Give the extent of all Plasmodium falciparum-infected red blood cells.
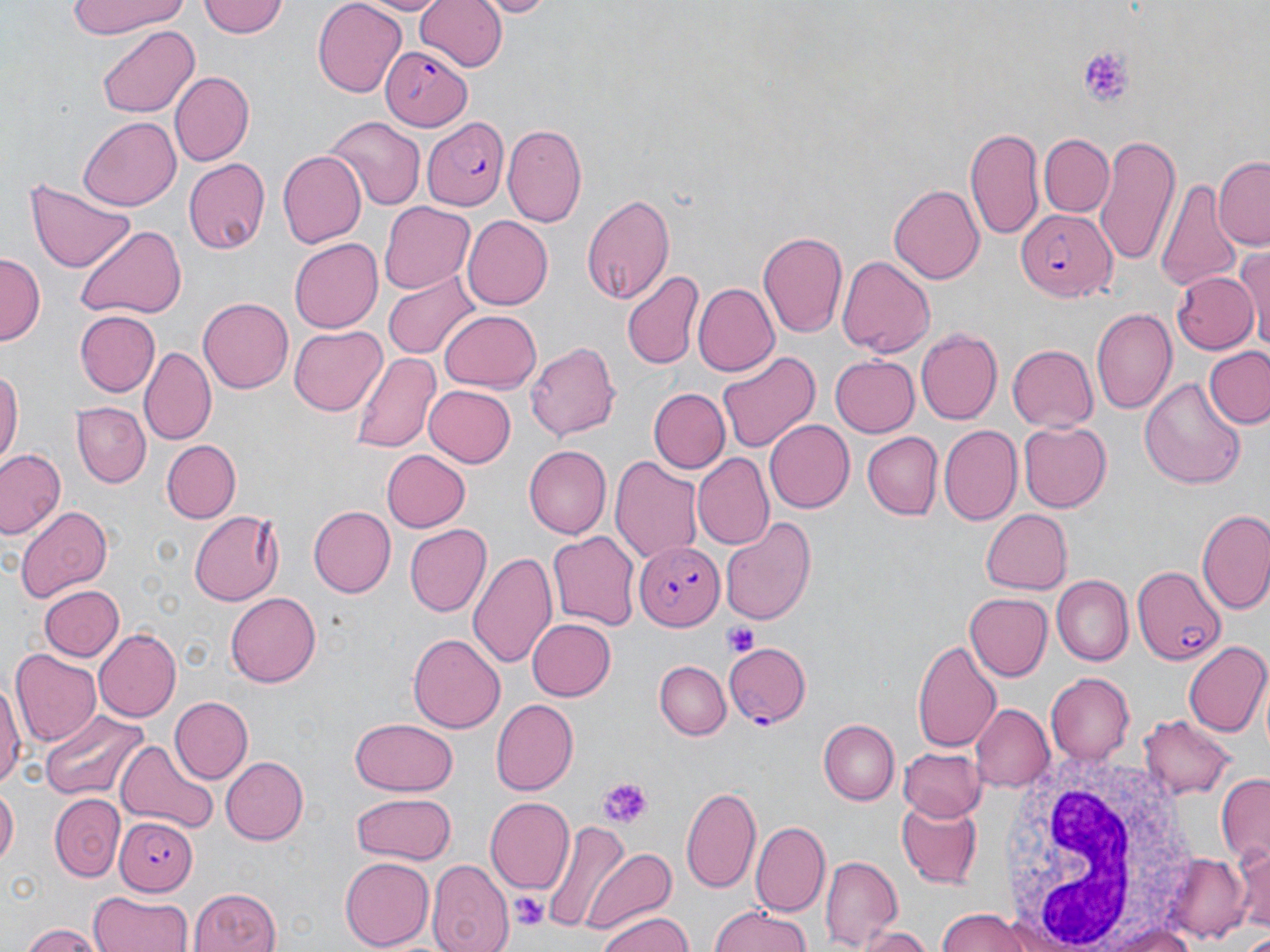

Approximate bounding boxes as (x1, y1, x2, y2) in pixels.
Plasmodium falciparum-infected red blood cells: (381, 47, 472, 131), (422, 118, 509, 211), (1018, 208, 1119, 299), (633, 542, 721, 630), (1132, 562, 1227, 667), (724, 640, 812, 728), (114, 814, 195, 894).

slide-level diagnosis = Plasmodium falciparum
modality = light microscopy
image size = 1270×952 pixels
preparation = thin blood film
stain = May-Grünwald-Giemsa
magnification = 1000x
platelet locations = approximate bounding boxes as (x1, y1, x2, y2) in pixels: (1077, 46, 1137, 107), (724, 622, 761, 658), (597, 779, 650, 824), (513, 893, 545, 930)
uninfected red blood cell locations = approximate bounding boxes as (x1, y1, x2, y2) in pixels: (67, 0, 194, 39), (199, 0, 289, 40), (312, 0, 406, 95), (355, 0, 452, 15), (414, 0, 508, 71), (475, 0, 555, 17), (97, 26, 199, 118), (170, 72, 254, 167), (81, 115, 180, 210), (325, 118, 422, 209), (502, 123, 588, 225), (964, 124, 1045, 239), (1040, 134, 1114, 217), (1093, 134, 1182, 270), (278, 149, 366, 250), (1215, 156, 1270, 248), (183, 158, 270, 255), (1157, 176, 1242, 295), (26, 180, 137, 273), (889, 182, 984, 285), (580, 191, 676, 304), (378, 201, 475, 295), (461, 215, 552, 310), (73, 225, 188, 322), (758, 231, 849, 341), (289, 238, 384, 333), (1234, 242, 1270, 348), (1, 253, 43, 346), (835, 254, 935, 359), (382, 267, 480, 360), (621, 269, 705, 370), (1170, 272, 1258, 354), (693, 282, 779, 377), (198, 296, 292, 391), (1092, 305, 1178, 417), (75, 311, 160, 395), (439, 311, 541, 394), (290, 326, 385, 414), (915, 329, 1003, 426), (525, 339, 622, 441), (1007, 344, 1098, 434), (140, 346, 215, 443), (1205, 347, 1270, 429), (715, 348, 822, 454), (350, 350, 440, 453), (830, 356, 920, 436), (0, 363, 22, 466), (1140, 378, 1247, 489), (423, 383, 515, 466), (648, 387, 730, 473), (73, 403, 151, 487), (765, 419, 855, 514), (1017, 420, 1109, 513), (937, 425, 1021, 526), (862, 432, 943, 520), (161, 440, 240, 522), (523, 446, 610, 539), (0, 447, 65, 540), (380, 450, 470, 533), (610, 454, 705, 564), (693, 454, 773, 550), (14, 504, 114, 601), (310, 505, 394, 596), (978, 509, 1071, 595), (188, 511, 284, 605), (1197, 511, 1270, 617), (720, 517, 815, 624), (405, 523, 491, 616), (549, 530, 641, 632), (468, 548, 559, 670), (1052, 575, 1131, 665), (39, 585, 124, 663), (963, 592, 1051, 681), (226, 593, 321, 688), (525, 617, 615, 702), (93, 627, 180, 723), (407, 633, 505, 734), (913, 638, 1003, 756), (1185, 642, 1270, 741), (10, 648, 101, 746), (655, 661, 731, 741), (1044, 673, 1134, 765), (0, 678, 23, 791), (170, 697, 253, 784), (490, 698, 577, 794), (971, 703, 1052, 790), (42, 713, 149, 800), (1140, 713, 1232, 799), (351, 715, 456, 794), (819, 720, 900, 805), (118, 738, 216, 836), (900, 746, 988, 820), (219, 756, 307, 844), (1215, 773, 1270, 865), (0, 783, 18, 869), (682, 784, 763, 894), (47, 794, 129, 878), (353, 794, 455, 864), (485, 796, 574, 891), (897, 800, 982, 887), (752, 821, 830, 914), (542, 822, 642, 933), (581, 845, 677, 937), (1232, 845, 1270, 936), (1163, 854, 1249, 940), (819, 855, 901, 948), (340, 856, 433, 949), (426, 859, 513, 952), (184, 888, 283, 952), (88, 890, 193, 952), (708, 906, 816, 952), (847, 908, 931, 944), (933, 909, 1044, 952), (594, 910, 696, 952), (863, 922, 934, 952), (20, 923, 103, 952), (1104, 923, 1205, 952)
white blood cell locations = approximate bounding boxes as (x1, y1, x2, y2) in pixels: (993, 745, 1206, 950)
field of view = single